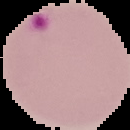
image type = cell region segmented out of the field of view; surrounding area masked to black
preparation = thin blood smear
malaria status = parasitized
image size = 130×130 pixels